Assess the morphology of the erythrocytes.
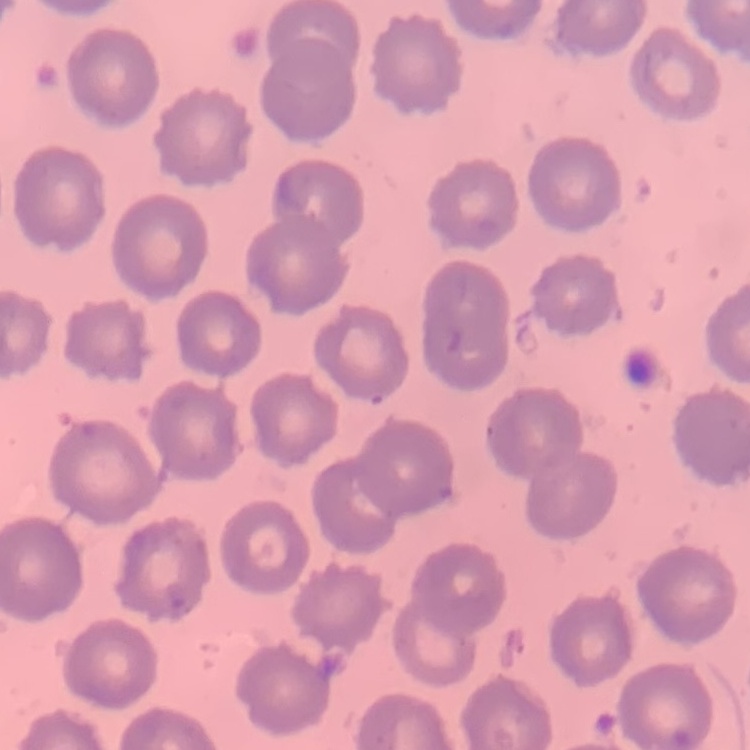

No rouleaux formation.

Field's or Giemsa stain. Thin blood film. Square crop of a larger photomicrograph.